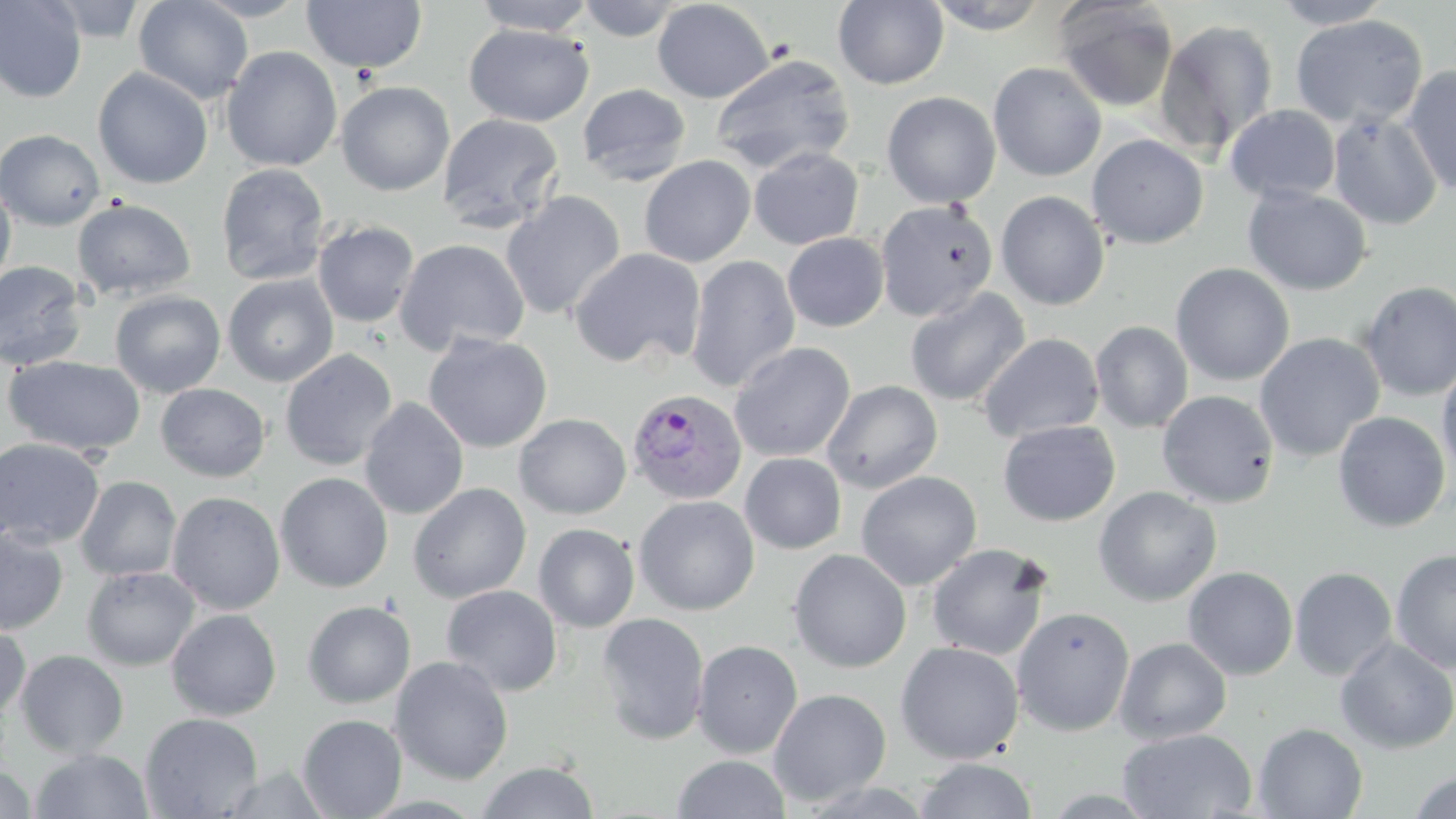

Summary:
  - Coordinate format: approximate bounding boxes as (x1,y1)-(x2,y2) corner pairs in pixels
  - Plasmodium vivax-infected red blood cell locations: (626,387)-(748,505)
  - Uninfected red blood cell locations: (0,0)-(87,103), (42,0)-(153,43), (134,0)-(253,104), (189,0)-(311,21), (473,0)-(597,36), (577,0)-(684,42), (652,0)-(774,103), (833,0)-(949,90), (925,0)-(1052,34), (302,1)-(427,74), (1054,1)-(1179,113), (1270,1)-(1395,28), (1290,14)-(1428,130), (1154,19)-(1279,157), (464,24)-(593,127), (221,46)-(342,172), (709,53)-(856,176), (988,62)-(1107,182), (1400,65)-(1456,196), (93,67)-(213,190), (336,81)-(455,196), (577,83)-(691,187), (881,91)-(1001,208), (1224,104)-(1341,204), (1328,112)-(1443,230), (437,113)-(564,234), (0,129)-(106,231), (1086,134)-(1209,249), (748,147)-(864,250), (767,148)-(875,333), (639,155)-(756,268), (216,164)-(330,285), (0,182)-(16,289), (1243,186)-(1373,296), (996,190)-(1110,310), (501,191)-(626,321), (72,198)-(197,301), (875,200)-(998,322), (312,220)-(420,328), (782,232)-(889,332), (394,238)-(530,356), (569,248)-(706,370), (685,254)-(800,392), (0,261)-(88,371), (1171,262)-(1295,386), (222,274)-(339,387), (1358,281)-(1456,401), (905,287)-(1030,407), (110,290)-(226,398), (1090,321)-(1194,433), (1254,332)-(1385,462), (423,333)-(553,453), (978,333)-(1104,444), (729,342)-(855,462), (279,349)-(398,471), (4,355)-(146,458), (1437,360)-(1456,483), (821,380)-(943,494), (156,383)-(270,482), (1157,390)-(1279,508), (359,397)-(469,519), (1332,411)-(1451,533), (514,413)-(631,519), (998,420)-(1120,526), (542,429)-(656,565), (0,438)-(105,548), (741,453)-(847,554), (855,471)-(982,590), (275,472)-(393,593), (75,476)-(181,581), (408,482)-(531,604), (1093,486)-(1222,607), (167,491)-(285,615), (634,496)-(759,615), (533,523)-(639,632), (0,526)-(68,635), (926,543)-(1053,662), (788,549)-(912,673), (1390,549)-(1456,673), (82,566)-(199,671), (1183,566)-(1298,681), (1290,567)-(1398,680), (441,584)-(563,697), (302,600)-(416,708), (1011,607)-(1135,736), (166,609)-(282,721), (596,612)-(710,746), (0,621)-(31,719), (1114,637)-(1232,744), (1334,637)-(1456,754), (691,640)-(803,758), (895,641)-(1024,764), (15,650)-(129,758), (390,656)-(513,785), (769,688)-(892,807), (140,712)-(263,819), (297,714)-(407,819), (1253,723)-(1368,819), (1118,728)-(1257,819), (31,748)-(153,818), (672,755)-(791,818), (914,758)-(1037,818), (476,760)-(599,819), (0,765)-(37,818), (1407,771)-(1456,819)
  - Slide-level diagnosis: Plasmodium vivax
  - Stain: May-Grünwald-Giemsa
  - Modality: optical microscopy
  - Preparation: thin blood smear
  - Field of view: one of a larger specimen
  - Image size: 1456×819 pixels
  - Magnification: 1000x